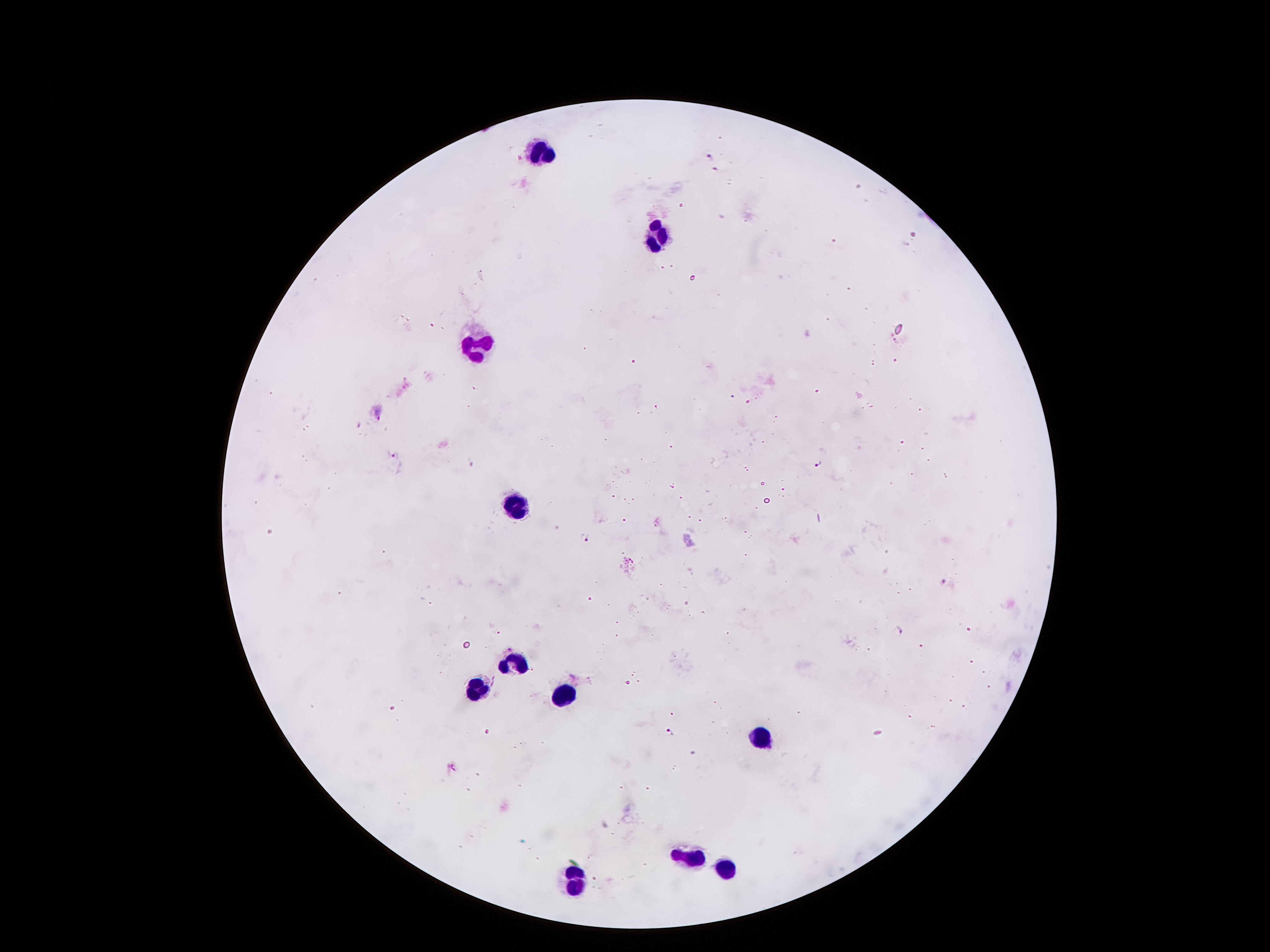
Approximate centers as [x, y] in pixels.
Summary:
  - Plasmodium parasite locations: [710, 158], [913, 237], [378, 417], [393, 457], [819, 464], [473, 465], [585, 537], [944, 581], [900, 632], [670, 732], [453, 767]
  - Leukocyte locations: [539, 154], [656, 237], [470, 344], [520, 507], [515, 666], [477, 688], [565, 698], [758, 736], [685, 856], [729, 866], [578, 879]
  - Image size: 1270×952 pixels
  - Preparation: thick blood smear
  - Capture: smartphone through the microscope eyepiece
  - Stain: Giemsa
  - Patient malaria status: infected with Plasmodium falciparum
  - Field of view: single
  - Magnification: 100x